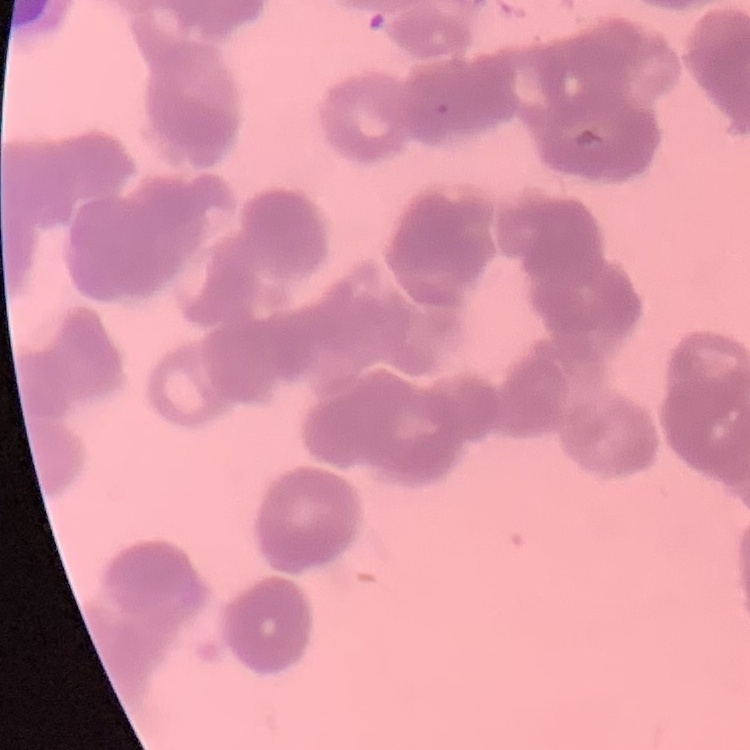
Summary:
  - Red blood cell morphology: rouleaux formation
  - Image type: square crop of a larger photomicrograph
  - Preparation: thin blood film
  - Stain: Field's or Giemsa